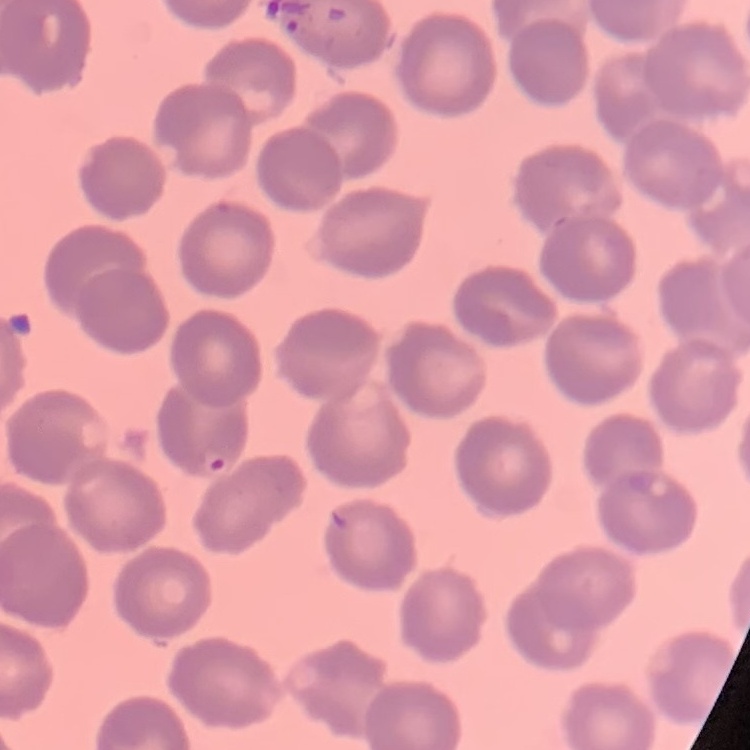
erythrocyte_morphology: no rouleaux formation
stain: Field's or Giemsa
image_type: square crop of a larger photomicrograph
preparation: thin blood smear